Give the extent of all Plasmodium falciparum-infected red blood cells.
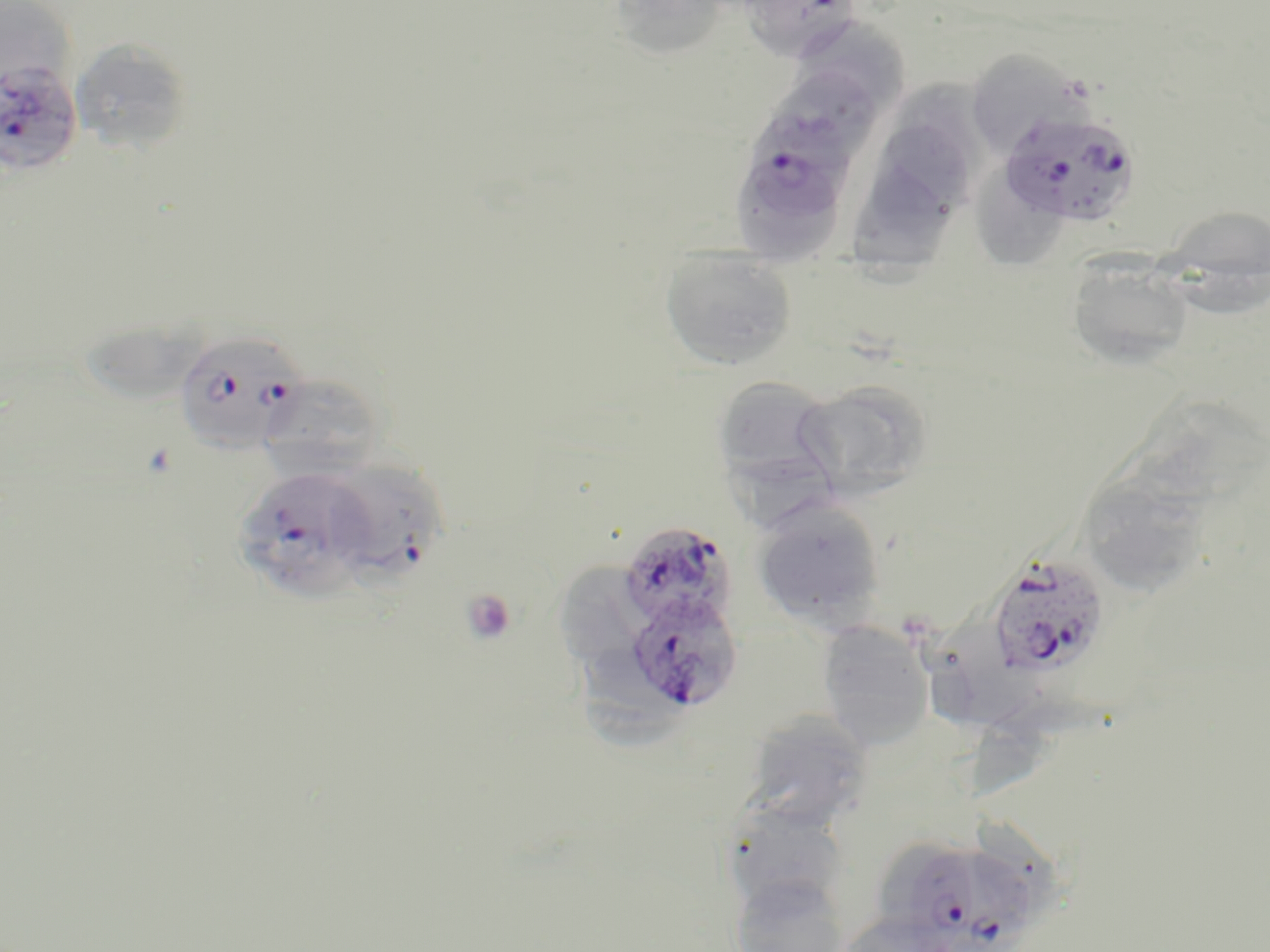

Approximate bounding boxes as (x1, y1, x2, y2) in pixels.
Plasmodium falciparum-infected red blood cells: (740, 0, 864, 60), (0, 60, 82, 178), (999, 108, 1143, 228), (729, 156, 853, 259), (171, 330, 312, 455), (331, 461, 442, 592), (235, 465, 384, 602), (618, 520, 736, 631), (986, 552, 1111, 680), (624, 592, 743, 713), (909, 847, 1044, 952).

Uninfected red blood cell locations: (605, 0, 736, 61), (0, 2, 74, 96), (792, 16, 909, 108), (71, 38, 193, 155), (962, 48, 1088, 158), (778, 73, 880, 157), (897, 80, 993, 188), (874, 128, 970, 240), (982, 158, 1062, 270), (857, 174, 953, 292), (1169, 203, 1270, 280), (659, 246, 797, 371), (1067, 256, 1195, 371), (1175, 256, 1270, 326), (81, 307, 206, 408), (258, 374, 386, 477), (711, 374, 843, 498), (797, 379, 933, 500), (1140, 398, 1266, 513), (1082, 474, 1203, 596), (752, 498, 886, 630), (563, 551, 664, 662), (929, 611, 1039, 731), (817, 621, 934, 750), (583, 640, 683, 751), (973, 692, 1114, 805), (741, 709, 875, 829), (720, 798, 853, 919), (729, 874, 851, 952), (835, 911, 956, 952). Platelet locations: (460, 588, 518, 647). Slide-level diagnosis: Plasmodium falciparum. Image is 1270×952 pixels. Light microscopy. Thin blood film. 1000x magnification. One field of a larger specimen. May-Grünwald-Giemsa-stained preparation.